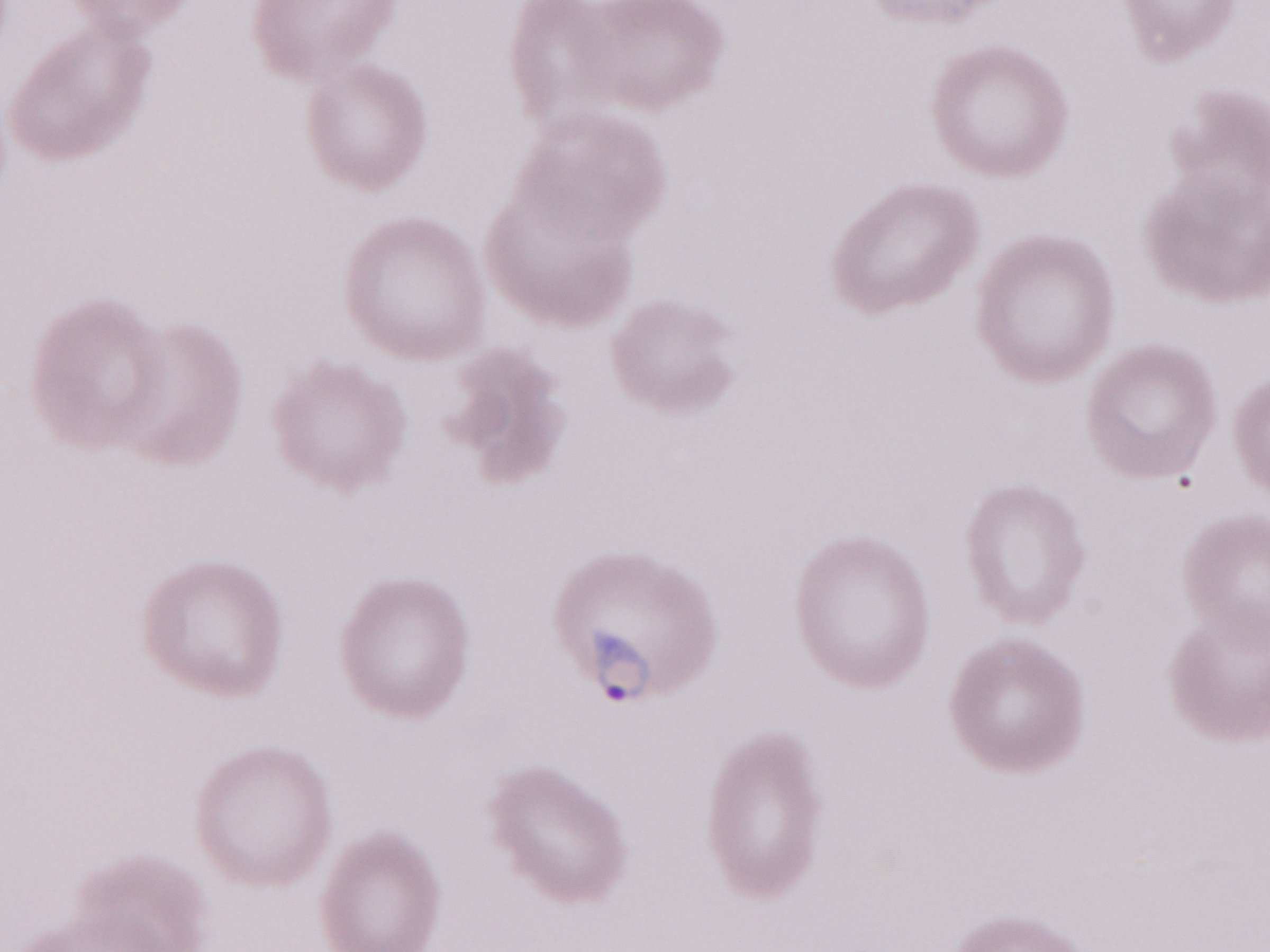

Single field of view. Magnification: 1,000x. Olympus BX43 microscope, Olympus DP73 camera. May-Grünwald-Giemsa-stained preparation. Thin peripheral-blood smear. Image is 1270×952 pixels. Patient diagnosis: malaria infection.